Classify this cell by malaria status.
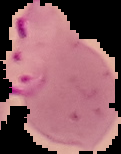

It is parasitized.

From a thin blood smear. Image is 121×154 pixels. Cell region segmented out of the field of view; the surrounding area is masked to black.